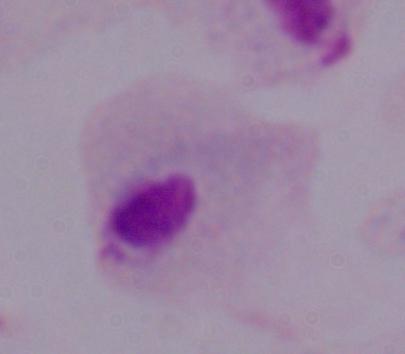

{
  "modality": "micrograph",
  "identification": "trichomonad",
  "magnification": "1000x"
}